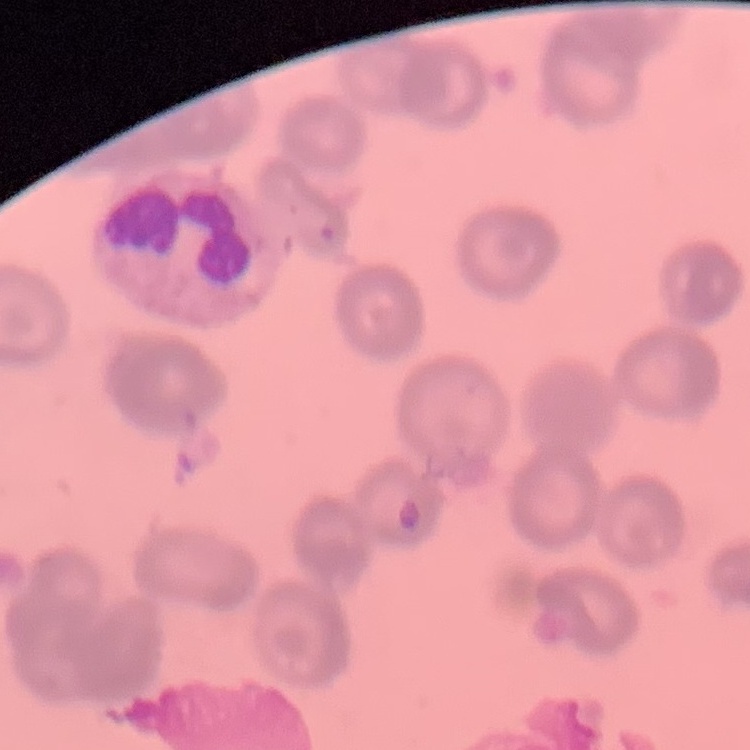

The red blood cells exhibit rouleaux formation. One tile cut from a larger photomicrograph. Thin peripheral smear. Stained with either Field's or Giemsa.